Point out each leukocyte.
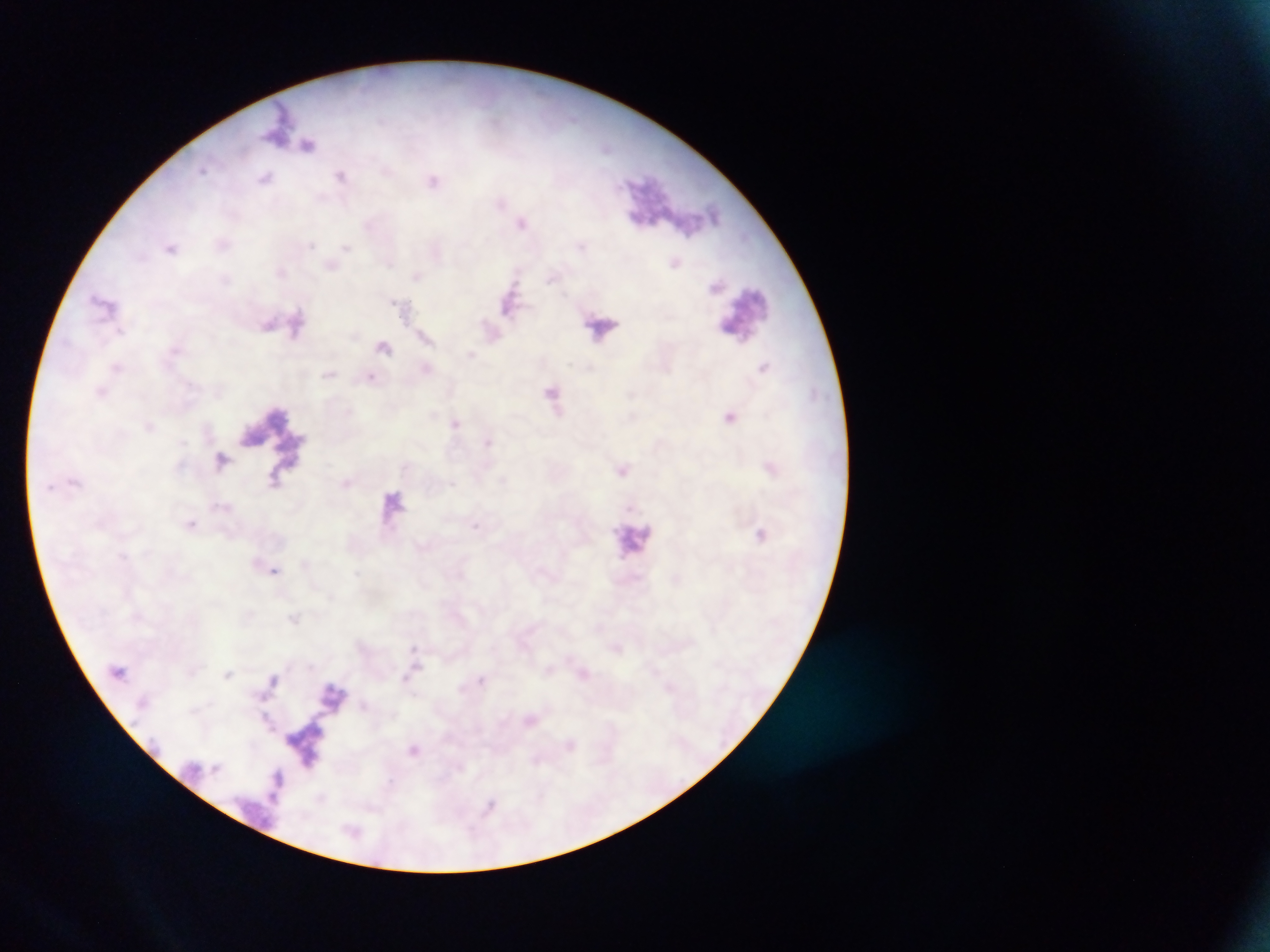

No leukocytes observed.

Approximate centers as [x, y] in pixels.
Summary:
  - Malaria parasite locations: [203, 170], [341, 175], [433, 180], [311, 244], [171, 246], [345, 248], [417, 276], [103, 301], [393, 302], [270, 323], [120, 330], [371, 377], [222, 461], [453, 484], [192, 523], [475, 526], [276, 570], [415, 647]
  - Country: Ghana
  - Field of view: single
  - Capture: mobile-phone photograph through a microscope
  - Image size: 1270×952 pixels
  - Preparation: thick blood film